Draw a bounding box around every leukocyte (white blood cell).
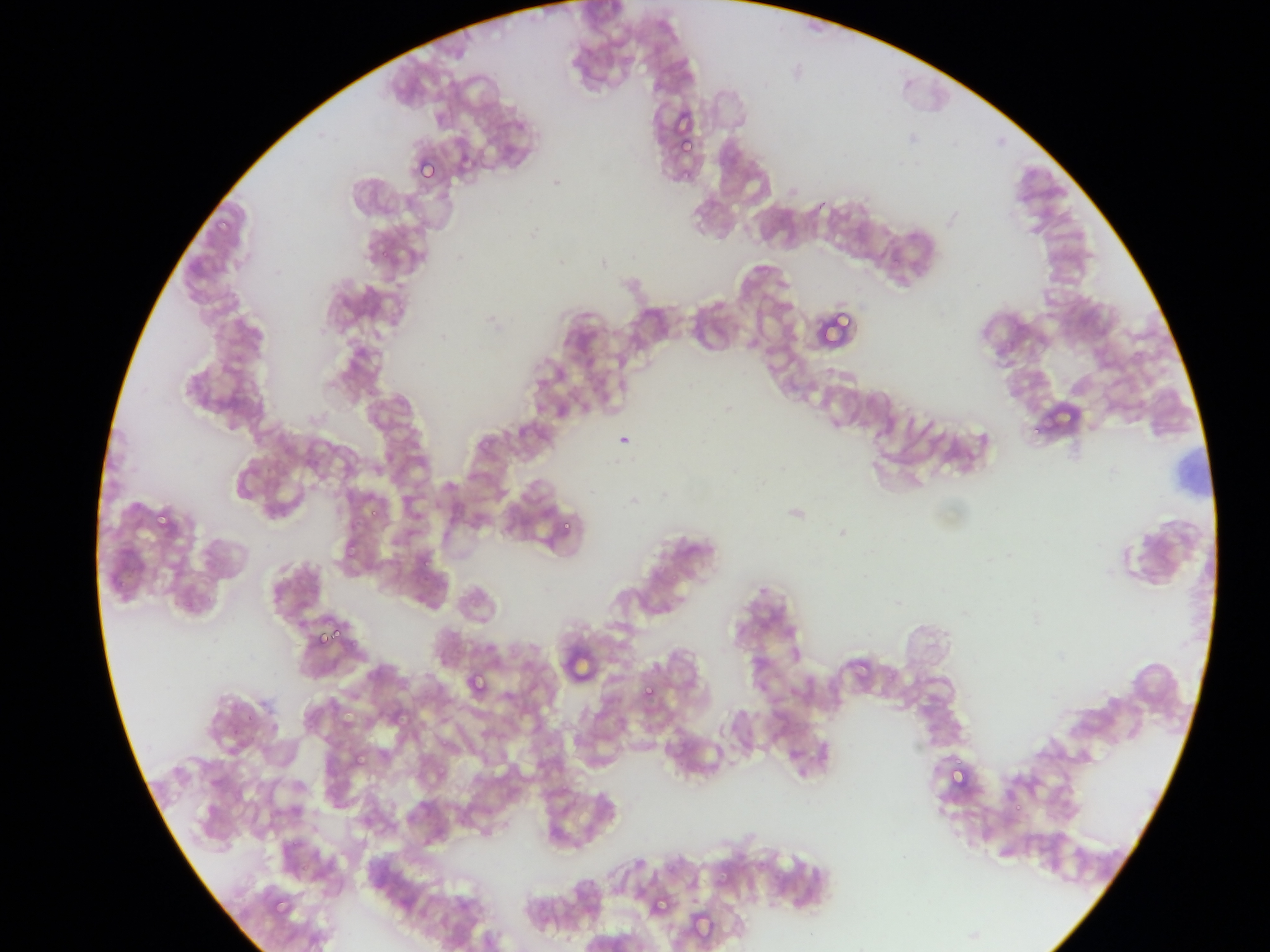

No leukocytes observed.

{
  "preparation": "thin blood smear",
  "field_of_view": "single",
  "capture": "mobile-phone photograph through a microscope",
  "image_size": "1270×952 pixels",
  "plasmodium_parasite_locations": "approximate bounding boxes as [left, top, right, bottom] in pixels: [671, 112, 693, 126], [679, 143, 693, 154], [418, 158, 437, 181], [840, 207, 852, 219], [830, 302, 856, 331], [153, 506, 166, 527], [369, 509, 383, 518], [562, 518, 577, 530], [341, 541, 357, 558], [423, 560, 430, 571], [331, 629, 341, 641], [318, 631, 322, 647], [469, 672, 484, 692], [641, 683, 656, 700], [393, 708, 417, 726], [352, 748, 366, 765], [952, 766, 970, 785], [719, 869, 732, 881], [655, 893, 667, 912], [275, 898, 295, 918], [690, 913, 716, 939]",
  "country": "Ghana"
}